Outline each blood parasite and name the species.
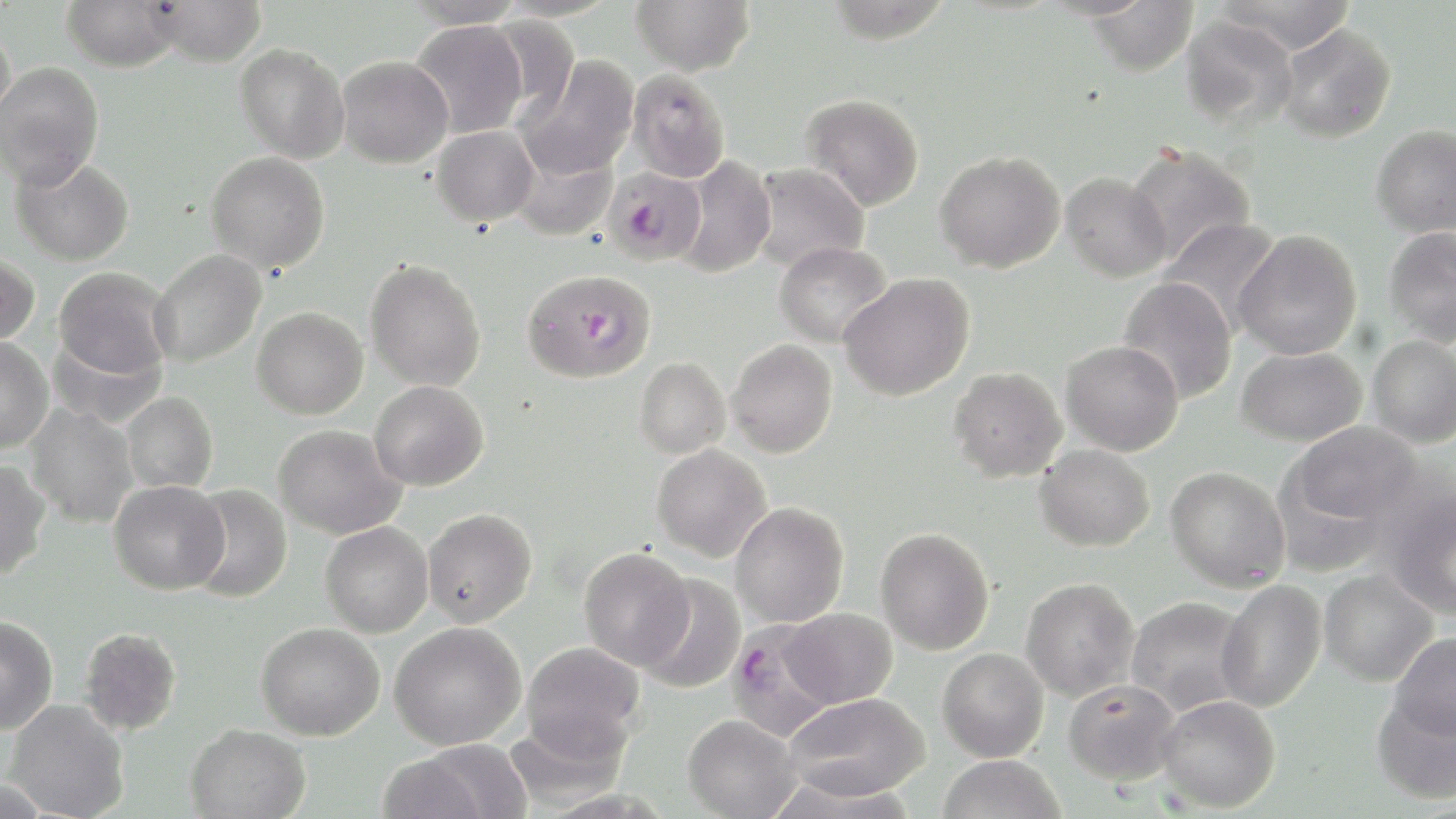

Approximate bounding boxes as (x1,y1)-(x2,y2) corner pairs in pixels.
Plasmodium falciparum-infected red blood cells: (605,167)-(704,265), (522,270)-(656,384), (724,622)-(840,741).
No Plasmodium ovale, Plasmodium malariae, Plasmodium vivax, Babesia divergens, or Trypanosoma brucei observed.

Summary:
  - Uninfected red blood cell locations: (62,0)-(182,72), (147,0)-(267,67), (402,0)-(528,28), (631,0)-(755,76), (825,0)-(952,44), (1214,0)-(1358,53), (1087,1)-(1198,76), (1181,14)-(1298,130), (486,16)-(579,121), (409,20)-(529,139), (1277,23)-(1396,143), (0,25)-(15,128), (235,42)-(350,163), (515,54)-(639,181), (336,56)-(453,168), (0,61)-(103,188), (627,69)-(730,183), (800,93)-(924,210), (1372,124)-(1456,237), (431,126)-(539,226), (510,144)-(618,242), (1122,144)-(1256,267), (935,150)-(1065,273), (206,152)-(330,273), (10,155)-(135,266), (676,156)-(776,278), (750,163)-(871,273), (1061,172)-(1171,282), (1159,218)-(1283,333), (1383,227)-(1456,346), (1233,230)-(1362,360), (774,241)-(893,347), (149,249)-(267,368), (0,253)-(40,345), (365,258)-(486,391), (53,267)-(174,379), (838,273)-(975,401), (1117,277)-(1238,404), (251,307)-(368,419), (48,331)-(166,429), (1367,335)-(1456,448), (0,337)-(53,452), (727,338)-(838,458), (1061,340)-(1184,456), (1235,347)-(1367,446), (634,357)-(730,459), (948,366)-(1067,482), (369,381)-(489,491), (121,391)-(218,494), (25,405)-(138,526), (1282,421)-(1424,539), (274,424)-(407,539), (652,443)-(772,562), (1035,444)-(1155,551), (0,459)-(52,579), (1165,466)-(1291,592), (109,480)-(230,595), (184,484)-(292,603), (1380,485)-(1456,621), (730,502)-(849,627), (422,508)-(538,627), (320,521)-(433,637), (875,527)-(994,655), (579,547)-(694,670), (1318,570)-(1438,687), (635,574)-(745,694), (1020,577)-(1140,701), (1215,579)-(1327,712), (1126,596)-(1252,716), (783,606)-(899,707), (0,615)-(58,734), (389,621)-(526,749), (256,622)-(385,741), (78,626)-(182,736), (1388,632)-(1456,740), (521,642)-(645,761), (937,648)-(1049,762), (1063,678)-(1181,785), (1371,687)-(1456,805), (784,692)-(931,801), (1155,694)-(1281,813), (5,699)-(130,819), (683,714)-(801,818), (185,723)-(310,818), (416,740)-(534,818), (376,752)-(491,819), (937,755)-(1065,819), (0,776)-(52,819)
  - Slide-level diagnosis: Plasmodium falciparum
  - Field of view: single
  - Magnification: 1000x
  - Modality: light microscopy
  - Preparation: thin blood smear
  - Stain: May-Grünwald-Giemsa
  - Image size: 1456×819 pixels